Name the blood parasite species.
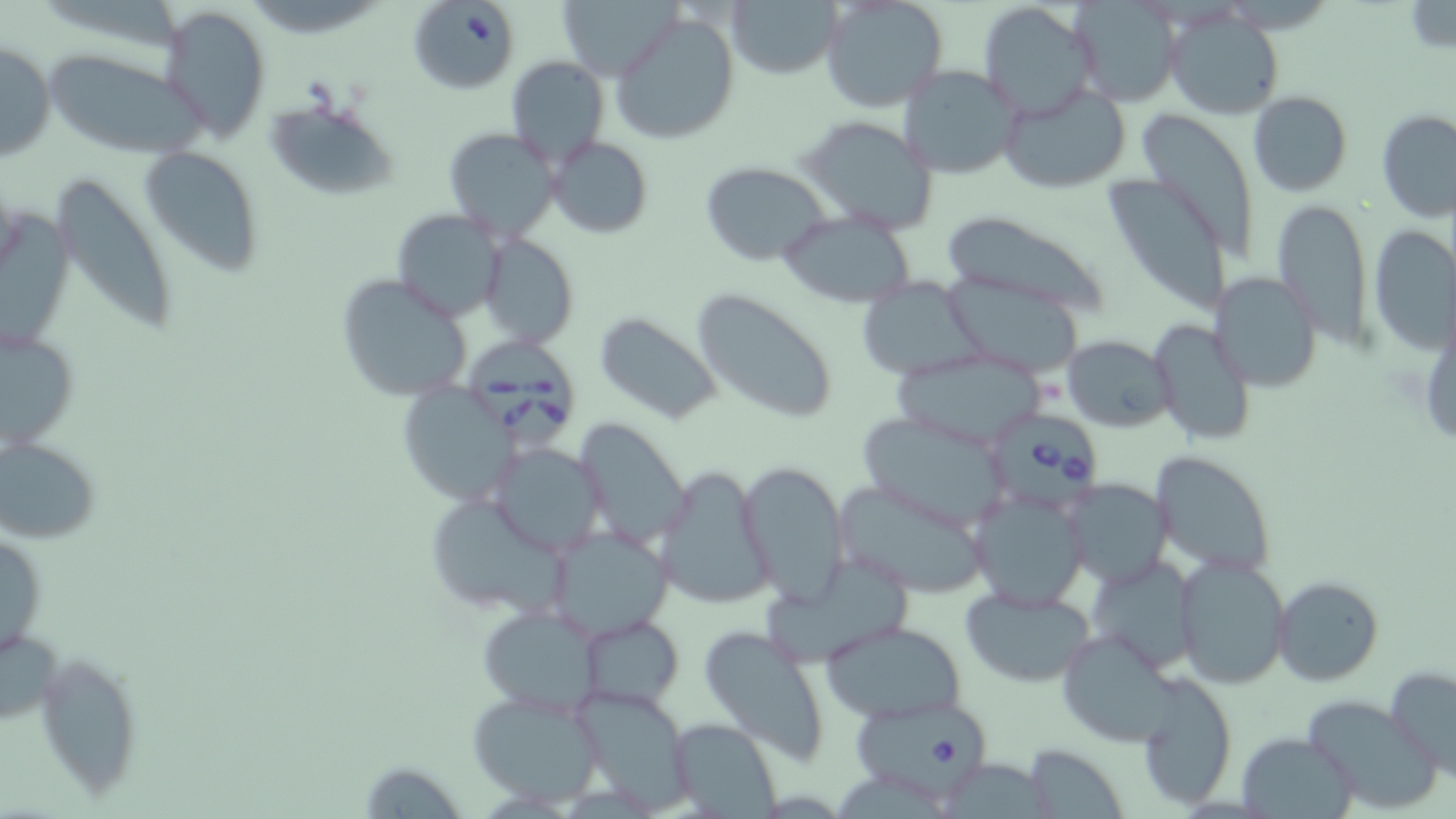
Babesia divergens.

Summary:
  - Coordinate format: approximate bounding boxes as (x1,y1)-(x2,y2) corner pairs in pixels
  - Babesia divergens-infected red blood cell locations: (466,341)-(577,452), (995,408)-(1102,512), (847,698)-(1000,799)
  - Uninfected red blood cell locations: (557,0)-(681,79), (728,0)-(844,79), (821,0)-(948,113), (1403,1)-(1456,53), (414,3)-(519,92), (975,3)-(1095,118), (1071,3)-(1182,106), (158,5)-(272,141), (1166,7)-(1284,119), (611,10)-(740,145), (1,39)-(55,164), (44,51)-(207,158), (505,56)-(607,166), (897,65)-(1024,179), (997,83)-(1133,192), (1247,90)-(1352,196), (266,98)-(398,201), (1376,109)-(1456,221), (1141,115)-(1266,269), (799,117)-(938,234), (442,128)-(559,241), (547,136)-(652,238), (139,143)-(263,273), (701,162)-(830,266), (53,172)-(178,344), (1107,173)-(1240,324), (1272,201)-(1372,348), (392,208)-(505,323), (940,209)-(1115,319), (778,212)-(918,307), (1368,224)-(1456,356), (478,234)-(577,348), (336,271)-(477,403), (1212,273)-(1322,391), (945,277)-(1082,378), (856,278)-(983,378), (691,290)-(841,425), (596,313)-(723,425), (1150,319)-(1256,447), (2,324)-(80,453), (1061,334)-(1175,433), (890,349)-(1047,449), (396,384)-(521,509), (856,413)-(1014,530), (571,418)-(691,549), (1,436)-(101,544), (487,443)-(606,556), (1152,451)-(1275,575), (738,460)-(851,604), (656,464)-(777,611), (831,478)-(993,597), (1061,478)-(1171,586), (970,487)-(1088,608), (424,494)-(571,617), (547,526)-(674,640), (1,530)-(47,664), (1173,555)-(1290,688), (1087,556)-(1200,670), (1272,576)-(1384,686), (959,584)-(1099,687), (478,603)-(603,717), (577,617)-(683,708), (820,622)-(966,723), (698,623)-(833,765), (0,625)-(62,728), (1054,629)-(1185,747), (37,649)-(143,798), (1385,665)-(1456,779), (1135,676)-(1237,809), (569,683)-(697,812), (466,689)-(604,806), (1301,694)-(1440,813), (668,717)-(782,818), (1237,732)-(1353,816), (1026,743)-(1128,818), (358,760)-(470,819)
  - Stain: May-Grünwald-Giemsa
  - Field of view: one of a larger specimen
  - Preparation: thin blood smear
  - Magnification: 1000x
  - Image size: 1456×819 pixels
  - Modality: light microscopy